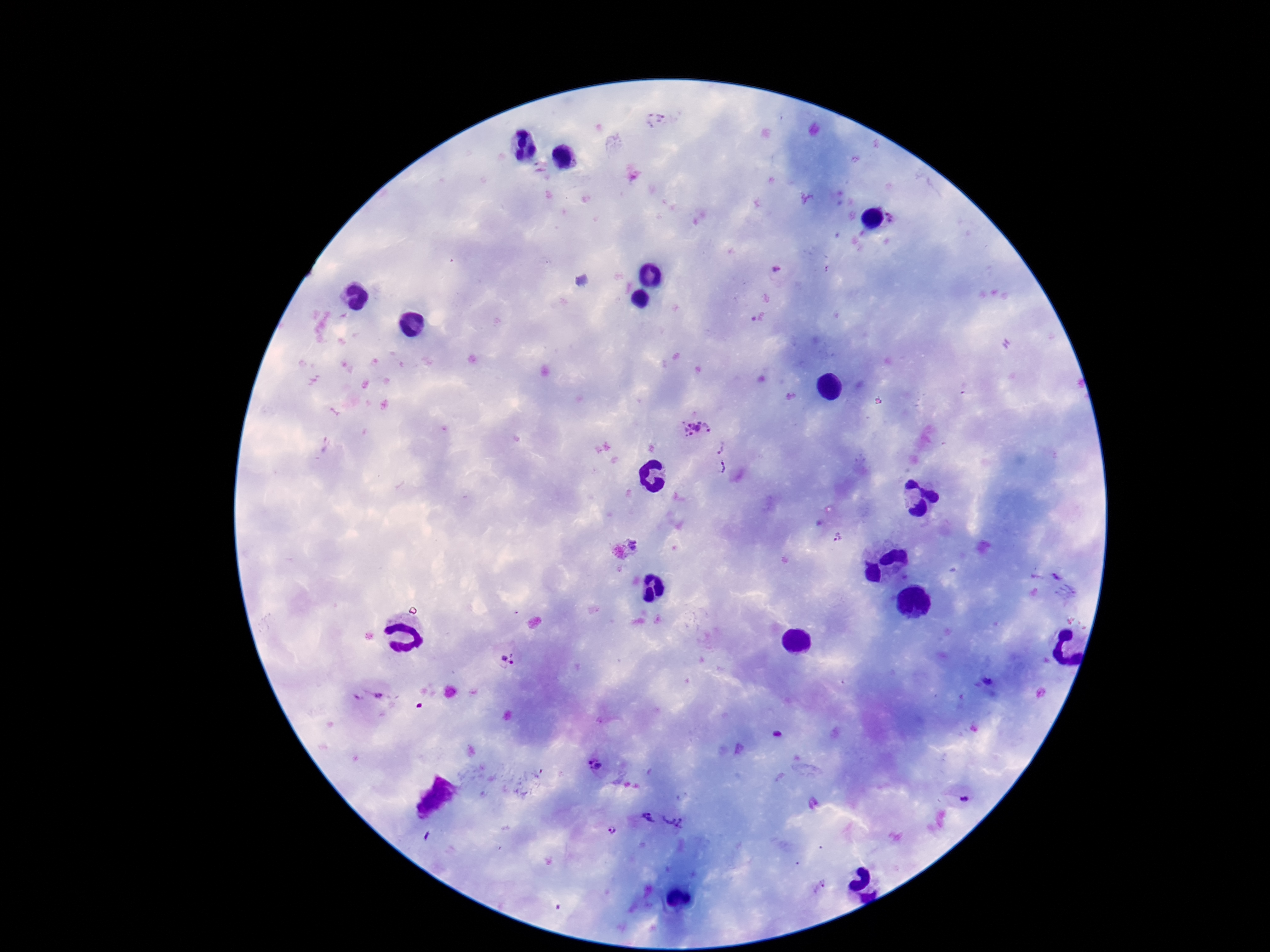
stain = Giemsa
patient malaria status = infected
image size = 1270×952 pixels
field of view = one from this slide
magnification = 100x
capture = smartphone camera through the microscope eyepiece
Plasmodium parasite locations = approximate object centers, in pixels from the top-left corner: (x=655, y=120), (x=895, y=215), (x=696, y=429), (x=723, y=448), (x=724, y=469), (x=838, y=538), (x=635, y=543), (x=1057, y=577), (x=508, y=659), (x=989, y=678), (x=367, y=697), (x=777, y=734), (x=595, y=765), (x=966, y=800), (x=647, y=819), (x=675, y=819), (x=611, y=830)
preparation = thick blood smear